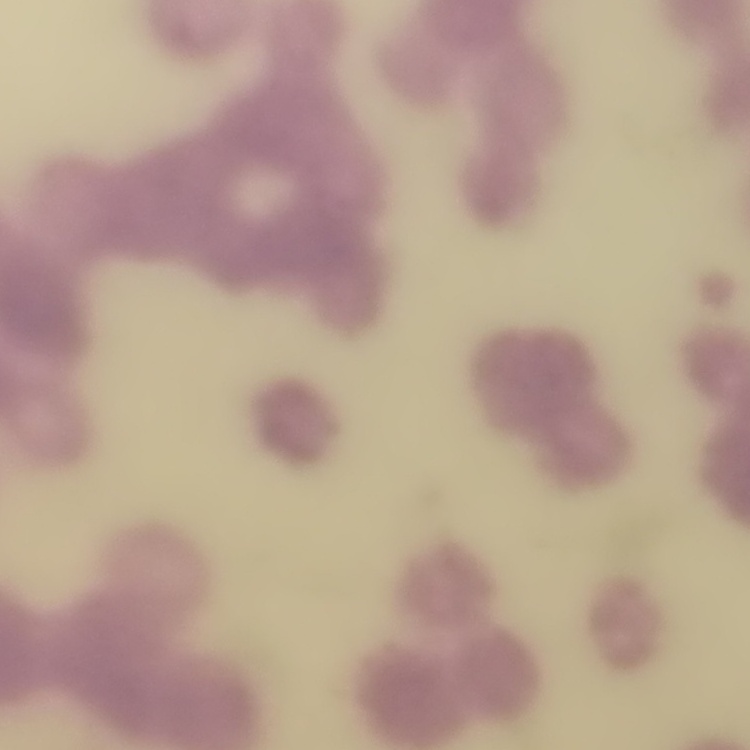

Summary:
  - Erythrocyte morphology: rouleaux formation
  - Stain: Field's or Giemsa
  - Image type: square crop of a larger photomicrograph
  - Preparation: thin blood smear